Name the parasite shown.
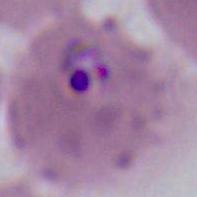

This is Plasmodium.

Summary:
  - Magnification: 400x or 1000x
  - Modality: photomicrograph